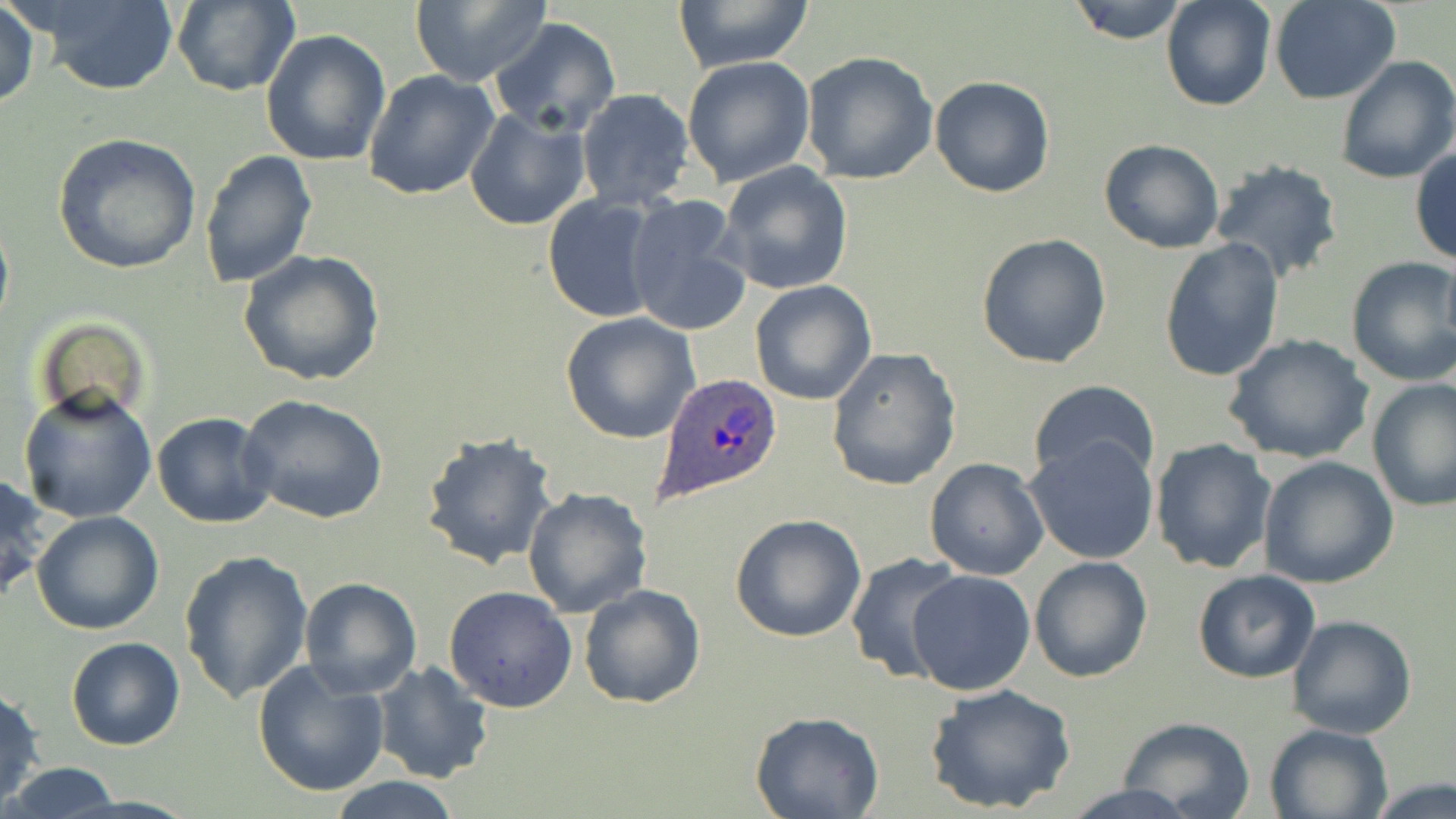 Approximate bounding boxes as [x1, y1, x2, y2] in pixels. Uninfected red blood cell locations: [409, 0, 549, 86], [671, 0, 815, 72], [1067, 0, 1189, 43], [1161, 0, 1277, 111], [1270, 0, 1402, 103], [1, 1, 41, 111], [170, 1, 301, 96], [24, 3, 180, 95], [488, 17, 622, 137], [260, 28, 392, 166], [800, 50, 939, 185], [681, 55, 815, 188], [1334, 55, 1456, 185], [363, 70, 499, 200], [929, 75, 1056, 198], [575, 89, 697, 210], [465, 107, 592, 232], [53, 132, 201, 273], [1098, 137, 1226, 254], [1410, 146, 1456, 266], [200, 148, 316, 289], [1208, 159, 1345, 284], [718, 160, 854, 295], [542, 195, 663, 323], [622, 197, 753, 335], [0, 206, 14, 343], [975, 233, 1112, 370], [1159, 237, 1287, 382], [1440, 246, 1456, 354], [238, 249, 386, 387], [1345, 255, 1456, 386], [749, 279, 876, 405], [560, 312, 700, 444], [1224, 335, 1372, 465], [828, 347, 962, 490], [1366, 377, 1455, 512], [1029, 378, 1160, 486], [18, 387, 158, 526], [238, 393, 388, 525], [152, 412, 277, 529], [421, 431, 559, 570], [1024, 439, 1159, 563], [1150, 439, 1276, 575], [1258, 455, 1398, 590], [923, 456, 1050, 581], [1, 473, 49, 605], [521, 486, 654, 619], [30, 511, 165, 635], [730, 514, 868, 644], [178, 551, 314, 708], [844, 551, 967, 687], [1028, 556, 1153, 684], [906, 569, 1036, 697], [1191, 570, 1321, 684], [298, 577, 422, 699], [578, 584, 707, 709], [443, 586, 577, 712], [1286, 615, 1419, 739], [67, 637, 185, 751], [250, 658, 391, 796], [370, 662, 496, 784], [924, 683, 1078, 814], [1, 685, 45, 805], [750, 712, 883, 819], [1115, 716, 1257, 819], [1263, 723, 1393, 819], [3, 764, 124, 817], [324, 775, 464, 818], [1367, 777, 1456, 818]. Plasmodium ovale-infected red blood cell locations: [655, 372, 784, 506]. Slide-level diagnosis: Plasmodium ovale. Captured at 1000x magnification. Image is 1456×819 pixels. Optical microscopy. Thin blood film. One field of a larger specimen. May-Grünwald-Giemsa stain.